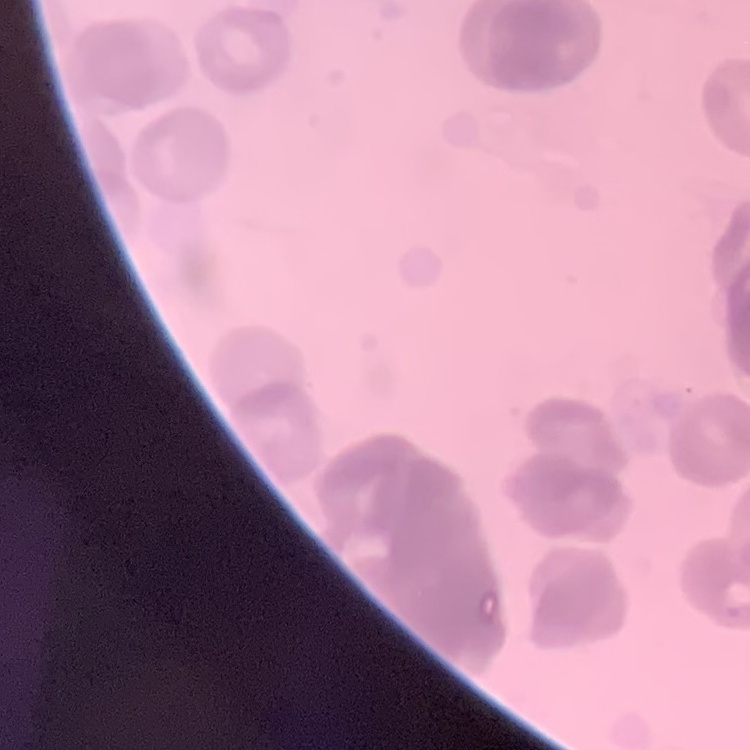
red_blood_cell_morphology: rouleaux formation
preparation: thin blood smear
stain: Field's or Giemsa
image_type: one tile cut from a larger photomicrograph